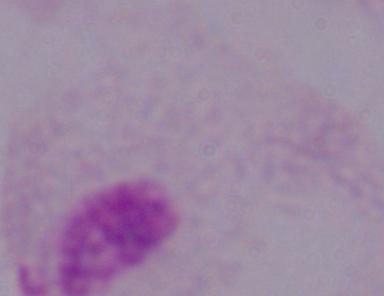
identification = trichomonad
magnification = 1000x
modality = micrograph